Classify this cell by malaria status.
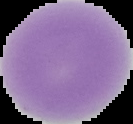
Uninfected.

Cell region segmented out of the field of view; the surrounding area is masked to black. Image is 133×124 pixels. From a thin blood film.